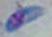 Toxoplasma gondii is seen. Captured at 1000x magnification. Photomicrograph.